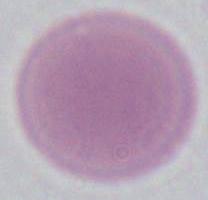
Photomicrograph. Captured at 1000x magnification. An erythrocyte is seen.